Locate every Plasmodium parasite.
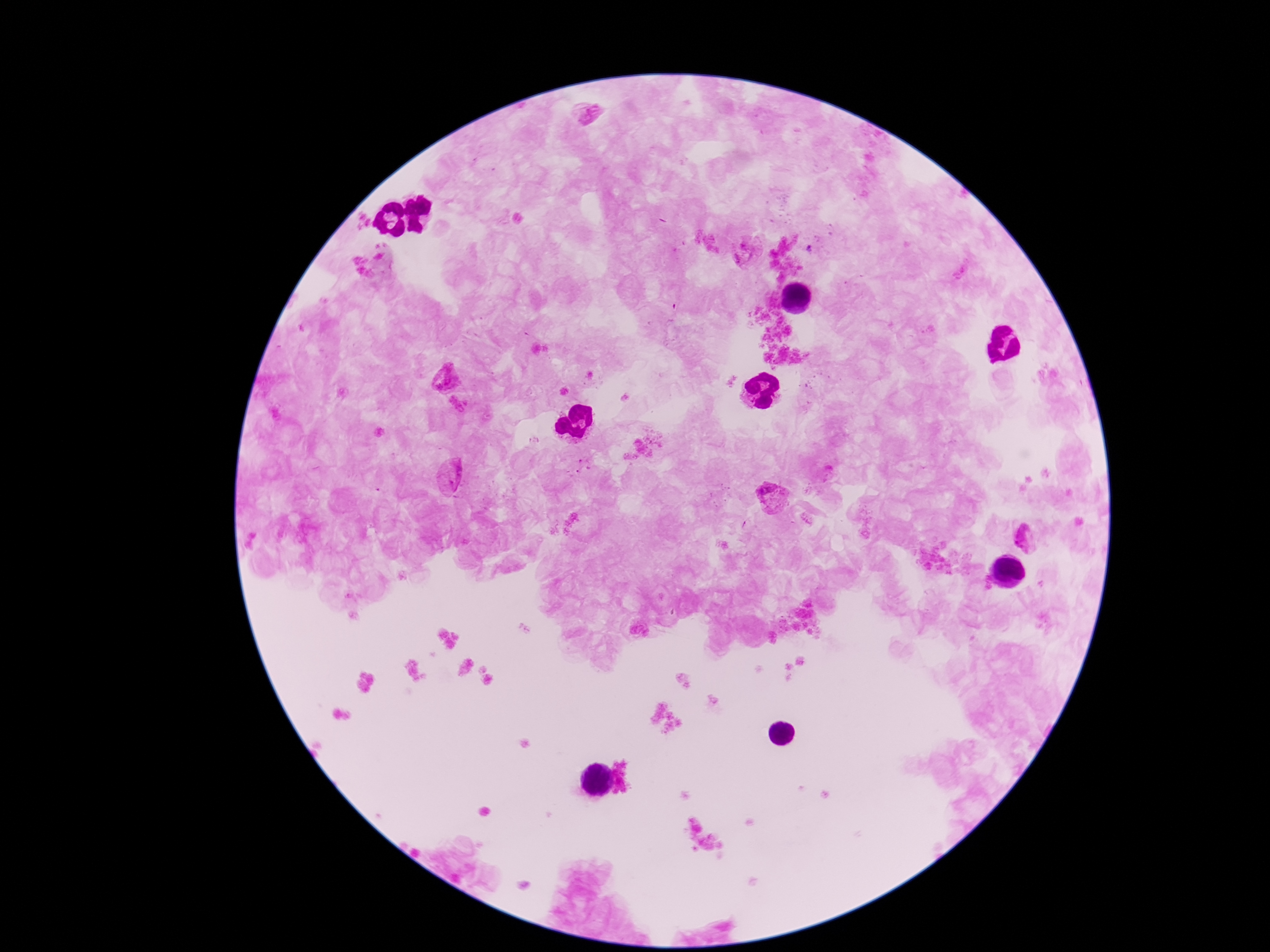

Approximate object centers, in pixels from the top-left corner.
Plasmodium parasites: (x=591, y=120), (x=747, y=251), (x=446, y=379), (x=450, y=476), (x=772, y=496), (x=1026, y=538).

Summary:
  - Patient malaria status: infected
  - Stain: Giemsa
  - Preparation: thick blood smear
  - Image size: 1270×952 pixels
  - Capture: smartphone camera through the microscope eyepiece
  - Field of view: single
  - Magnification: 100x